Give the extent of all Plasmodium malariae-infected red blood cells.
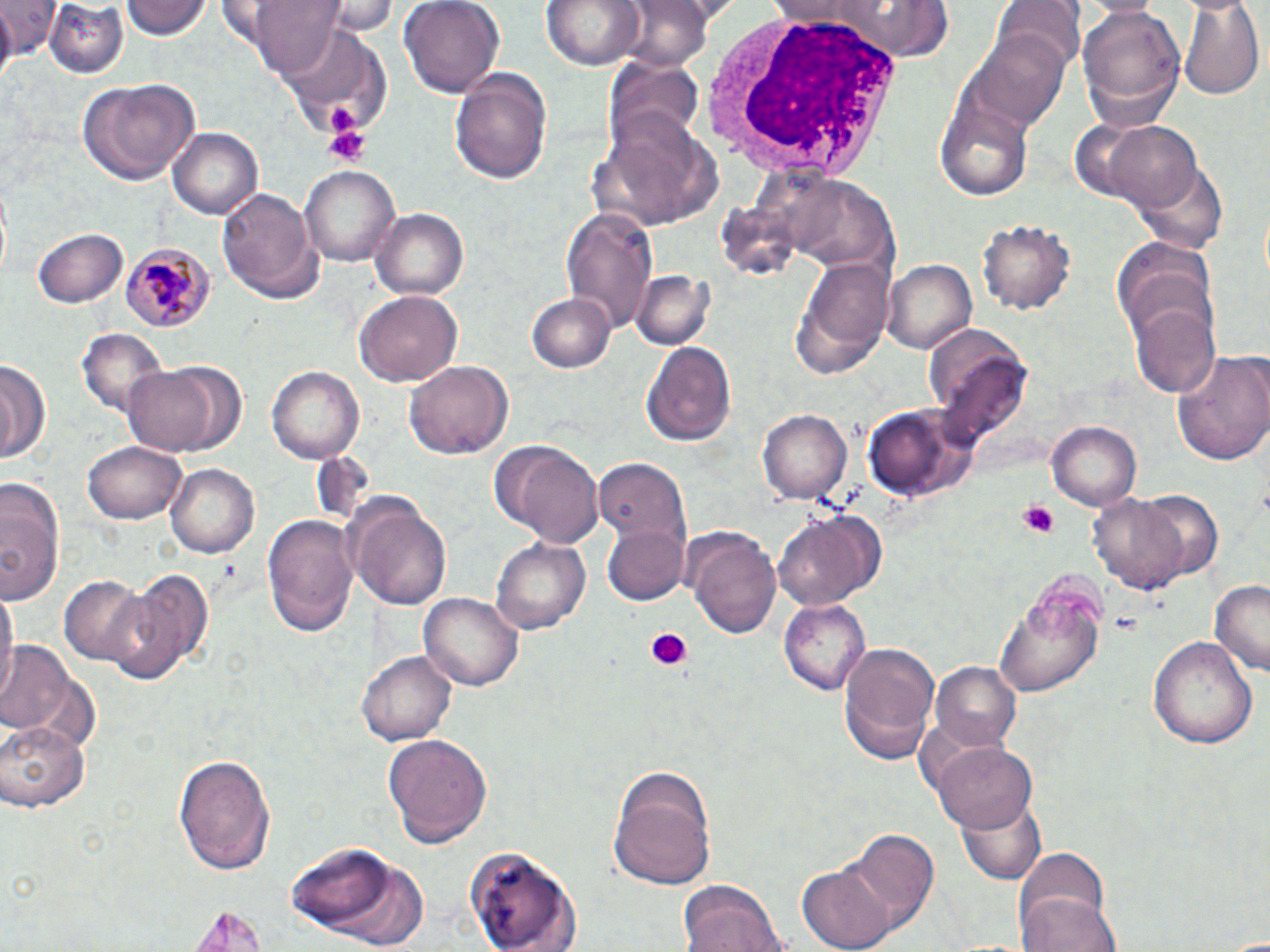

Approximate bounding boxes as named x1/y1/x2/y2 corners in pixels.
Plasmodium malariae-infected red blood cells: (x1=121, y1=239, x2=214, y2=331).

Uninfected red blood cell locations: (x1=0, y1=0, x2=61, y2=56), (x1=42, y1=0, x2=130, y2=76), (x1=122, y1=0, x2=210, y2=42), (x1=244, y1=0, x2=350, y2=77), (x1=322, y1=0, x2=401, y2=33), (x1=400, y1=0, x2=503, y2=93), (x1=542, y1=0, x2=644, y2=70), (x1=838, y1=0, x2=959, y2=59), (x1=995, y1=0, x2=1082, y2=75), (x1=1176, y1=0, x2=1263, y2=100), (x1=612, y1=1, x2=714, y2=72), (x1=1078, y1=4, x2=1186, y2=131), (x1=973, y1=28, x2=1072, y2=127), (x1=609, y1=59, x2=704, y2=149), (x1=451, y1=69, x2=553, y2=187), (x1=76, y1=77, x2=199, y2=187), (x1=937, y1=97, x2=1038, y2=201), (x1=1104, y1=121, x2=1204, y2=212), (x1=167, y1=125, x2=262, y2=219), (x1=1136, y1=158, x2=1226, y2=254), (x1=300, y1=164, x2=403, y2=267), (x1=797, y1=180, x2=898, y2=274), (x1=217, y1=186, x2=325, y2=303), (x1=560, y1=207, x2=659, y2=328), (x1=370, y1=208, x2=468, y2=300), (x1=978, y1=219, x2=1073, y2=315), (x1=34, y1=228, x2=128, y2=307), (x1=1114, y1=243, x2=1219, y2=348), (x1=789, y1=257, x2=893, y2=377), (x1=883, y1=260, x2=975, y2=355), (x1=629, y1=269, x2=714, y2=352), (x1=354, y1=290, x2=462, y2=389), (x1=528, y1=294, x2=616, y2=373), (x1=1131, y1=302, x2=1220, y2=398), (x1=930, y1=326, x2=1033, y2=433), (x1=73, y1=330, x2=164, y2=414), (x1=643, y1=340, x2=736, y2=447), (x1=1172, y1=349, x2=1270, y2=466), (x1=0, y1=358, x2=48, y2=465), (x1=121, y1=361, x2=245, y2=458), (x1=405, y1=362, x2=514, y2=461), (x1=266, y1=364, x2=367, y2=463), (x1=867, y1=401, x2=979, y2=502), (x1=758, y1=409, x2=850, y2=504), (x1=1049, y1=420, x2=1143, y2=510), (x1=82, y1=439, x2=186, y2=525), (x1=502, y1=441, x2=603, y2=546), (x1=595, y1=457, x2=691, y2=544), (x1=165, y1=462, x2=260, y2=557), (x1=0, y1=476, x2=64, y2=605), (x1=1132, y1=487, x2=1224, y2=581), (x1=346, y1=492, x2=453, y2=610), (x1=1090, y1=493, x2=1191, y2=595), (x1=262, y1=511, x2=358, y2=636), (x1=774, y1=511, x2=879, y2=610), (x1=601, y1=525, x2=688, y2=605), (x1=686, y1=528, x2=784, y2=641), (x1=492, y1=536, x2=591, y2=633), (x1=110, y1=568, x2=211, y2=682), (x1=59, y1=572, x2=151, y2=666), (x1=1210, y1=582, x2=1270, y2=675), (x1=0, y1=583, x2=17, y2=698), (x1=995, y1=585, x2=1103, y2=699), (x1=419, y1=593, x2=524, y2=693), (x1=781, y1=600, x2=872, y2=695), (x1=1150, y1=635, x2=1258, y2=750), (x1=0, y1=642, x2=77, y2=736), (x1=839, y1=642, x2=941, y2=765), (x1=356, y1=647, x2=457, y2=749), (x1=929, y1=663, x2=1024, y2=754), (x1=0, y1=718, x2=90, y2=813), (x1=384, y1=731, x2=492, y2=845), (x1=932, y1=740, x2=1036, y2=834), (x1=173, y1=751, x2=276, y2=874), (x1=607, y1=764, x2=717, y2=890), (x1=953, y1=795, x2=1049, y2=883), (x1=846, y1=829, x2=940, y2=931), (x1=284, y1=840, x2=414, y2=941), (x1=1011, y1=849, x2=1111, y2=944), (x1=467, y1=851, x2=577, y2=948), (x1=801, y1=863, x2=896, y2=950), (x1=676, y1=880, x2=785, y2=952), (x1=1021, y1=893, x2=1119, y2=952), (x1=187, y1=904, x2=266, y2=952). Platelet locations: (x1=326, y1=102, x2=364, y2=134), (x1=320, y1=123, x2=373, y2=165), (x1=1016, y1=499, x2=1061, y2=538), (x1=641, y1=627, x2=691, y2=674). White blood cell locations: (x1=699, y1=10, x2=906, y2=183). Slide-level diagnosis: Plasmodium malariae. Thin blood film. Light microscopy. Image is 1270×952 pixels. 1000x magnification. May-Grünwald-Giemsa stain. Single field of view.